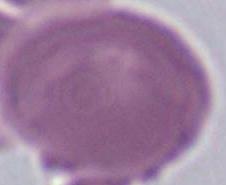
Photomicrograph. Captured at 1000x magnification. A red blood cell is shown.